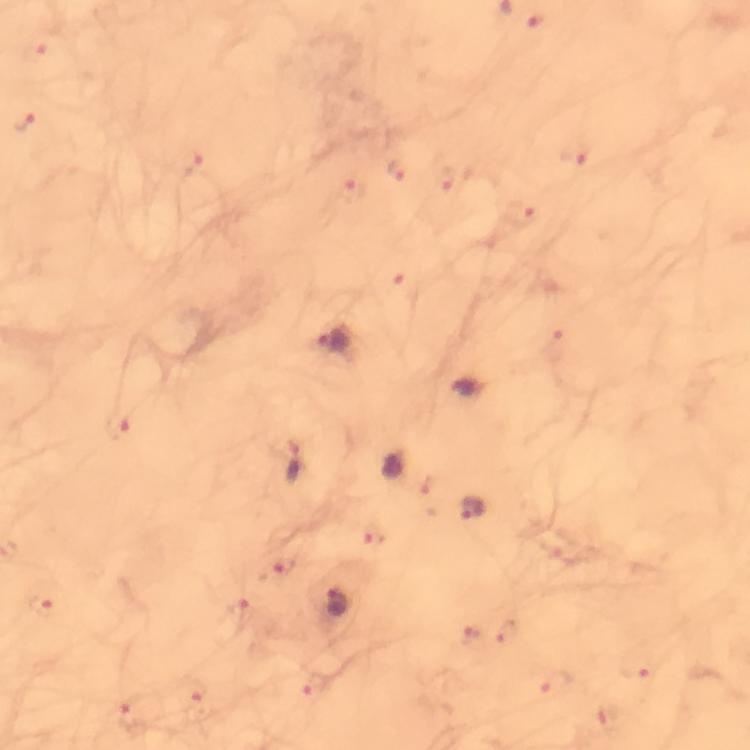 Approximate object centers, in pixels from the top-left corner. Plasmodium parasite locations: (x=335, y=342), (x=466, y=388), (x=294, y=464), (x=392, y=468), (x=473, y=510), (x=339, y=604). Photographed with a smartphone mounted on the microscope. Giemsa stain. Immersion oil was used. Cropped region of a single field of view. At 100x magnification. From a malaria diagnostic workup. Thick blood smear. Image is 750×750 pixels.